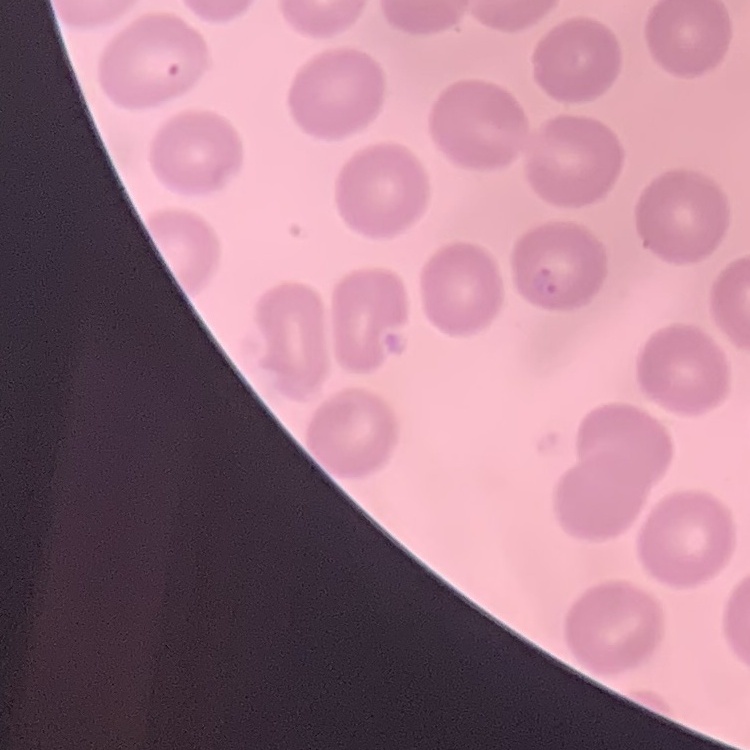
Summary:
  - Erythrocyte morphology: no rouleaux formation
  - Stain: Field's or Giemsa
  - Image type: one tile cut from a larger photomicrograph
  - Preparation: thin blood film